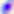

Summary:
  - Modality: micrograph
  - Magnification: 400x
  - Identification: Toxoplasma gondii